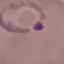
Summary:
  - Result: malaria parasites identified
  - Stain: Giemsa
  - Capture: smartphone camera at the microscope eyepiece
  - Image type: cell patch, automatically extracted from a larger field of view and resized to 64 × 64 pixels
  - Preparation: thin blood smear